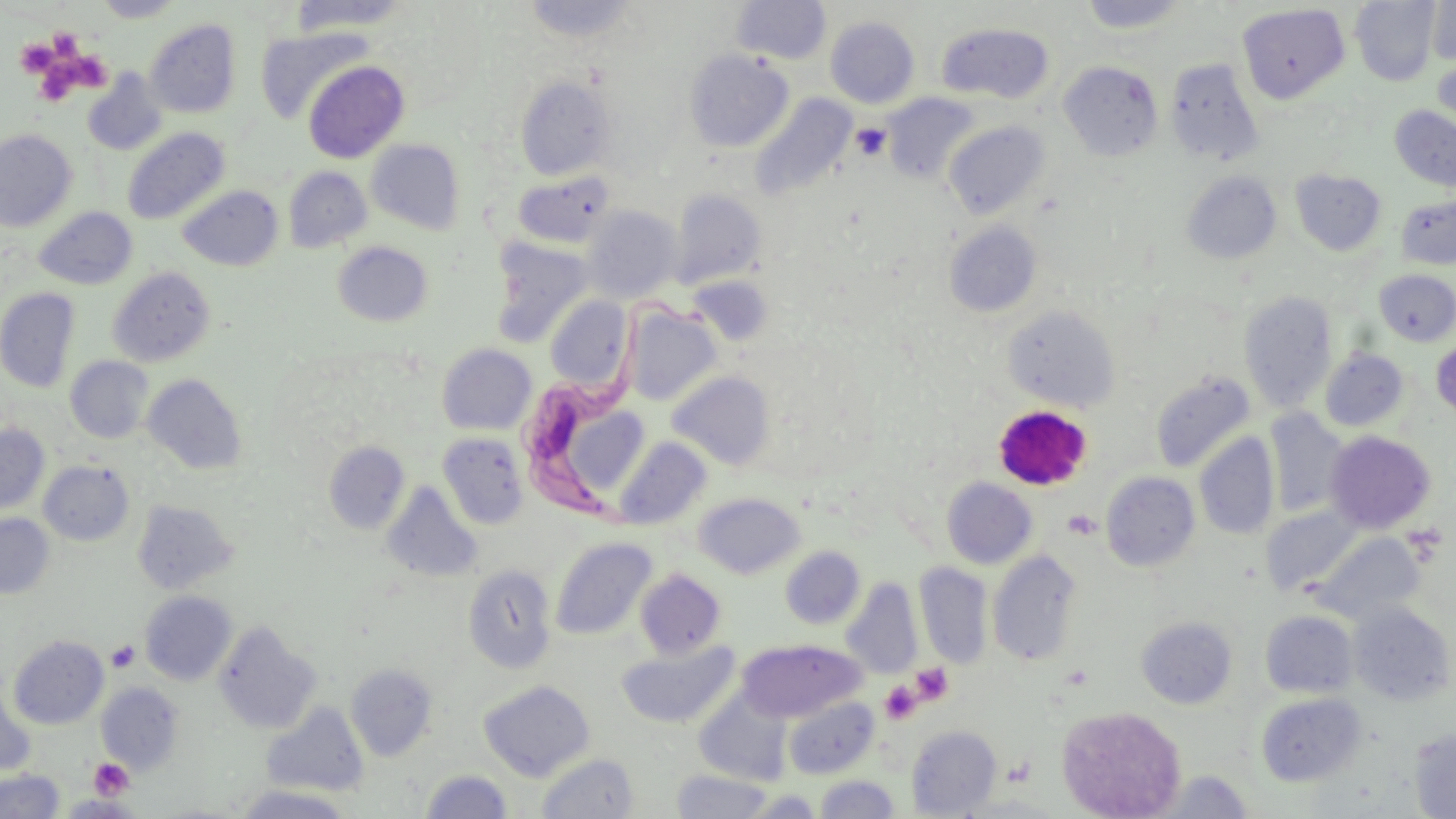
slide-level diagnosis = Trypanosoma brucei
image size = 1456×819 pixels
preparation = thin blood film
magnification = 1000x
modality = optical microscopy
field of view = one of a larger specimen
stain = May-Grünwald-Giemsa
uninfected red blood cell locations = approximate bounding boxes as [x1, y1, x2, y2] in pixels: [286, 0, 414, 36], [522, 0, 640, 43], [731, 0, 832, 64], [1350, 0, 1441, 85], [94, 1, 185, 22], [1076, 1, 1194, 34], [1426, 2, 1456, 67], [1238, 5, 1350, 103], [825, 16, 920, 108], [145, 20, 241, 118], [936, 23, 1054, 103], [256, 25, 371, 124], [684, 49, 793, 152], [1432, 54, 1456, 139], [1164, 58, 1265, 167], [303, 60, 410, 163], [1059, 61, 1164, 161], [83, 70, 167, 156], [516, 76, 617, 179], [881, 92, 981, 185], [750, 93, 857, 202], [1390, 106, 1456, 192], [943, 121, 1050, 220], [122, 128, 230, 225], [0, 129, 77, 232], [366, 140, 464, 233], [282, 166, 371, 253], [1291, 169, 1386, 255], [512, 170, 616, 249], [1182, 171, 1281, 264], [177, 185, 283, 271], [670, 190, 767, 287], [1396, 196, 1456, 269], [33, 207, 137, 289], [582, 207, 682, 302], [944, 222, 1042, 317], [490, 237, 593, 346], [333, 241, 433, 326], [108, 267, 215, 367], [1374, 269, 1456, 346], [689, 274, 774, 346], [0, 288, 80, 392], [1238, 290, 1337, 413], [545, 296, 632, 392], [1002, 304, 1121, 412], [624, 306, 721, 405], [1431, 338, 1456, 422], [436, 344, 537, 435], [1320, 348, 1409, 431], [65, 356, 154, 444], [667, 371, 776, 471], [1150, 371, 1255, 473], [142, 373, 247, 475], [569, 409, 649, 487], [1265, 411, 1349, 517], [0, 424, 49, 515], [1324, 430, 1436, 533], [437, 432, 528, 529], [1194, 433, 1279, 540], [614, 436, 712, 529], [323, 441, 410, 534], [38, 460, 134, 546], [1101, 471, 1200, 572], [942, 477, 1037, 568], [382, 481, 482, 583], [694, 492, 805, 579], [133, 499, 238, 594], [1263, 505, 1366, 595], [0, 513, 54, 599], [1310, 532, 1425, 623], [550, 537, 657, 641], [780, 546, 865, 629], [987, 550, 1084, 666], [914, 562, 993, 668], [462, 564, 557, 674], [634, 569, 727, 660], [842, 579, 923, 678], [140, 591, 237, 685], [1349, 602, 1454, 706], [1260, 610, 1357, 698], [1136, 616, 1236, 708], [214, 621, 321, 733], [9, 635, 109, 729], [737, 639, 865, 722], [619, 640, 739, 729], [346, 663, 437, 761], [478, 680, 595, 781], [96, 682, 184, 774], [0, 685, 36, 776], [1255, 692, 1367, 786], [694, 694, 790, 784], [782, 696, 879, 779], [262, 703, 368, 796], [1057, 705, 1187, 819], [906, 726, 1002, 816], [1410, 728, 1456, 818], [536, 752, 639, 818], [0, 769, 65, 818], [420, 769, 513, 818], [672, 769, 774, 818], [1157, 770, 1254, 818], [814, 775, 900, 818], [235, 784, 355, 818], [744, 789, 824, 818], [58, 795, 141, 817]
platelet locations = approximate bounding boxes as [x1, y1, x2, y2] in pixels: [49, 35, 81, 59], [14, 39, 59, 78], [72, 53, 118, 95], [39, 68, 79, 100], [851, 123, 891, 161], [993, 404, 1092, 489], [108, 641, 140, 672], [910, 663, 953, 705], [880, 681, 921, 724], [89, 758, 134, 800]
Trypanosoma brucei locations = approximate bounding boxes as [x1, y1, x2, y2] in pixels: [520, 306, 707, 520]